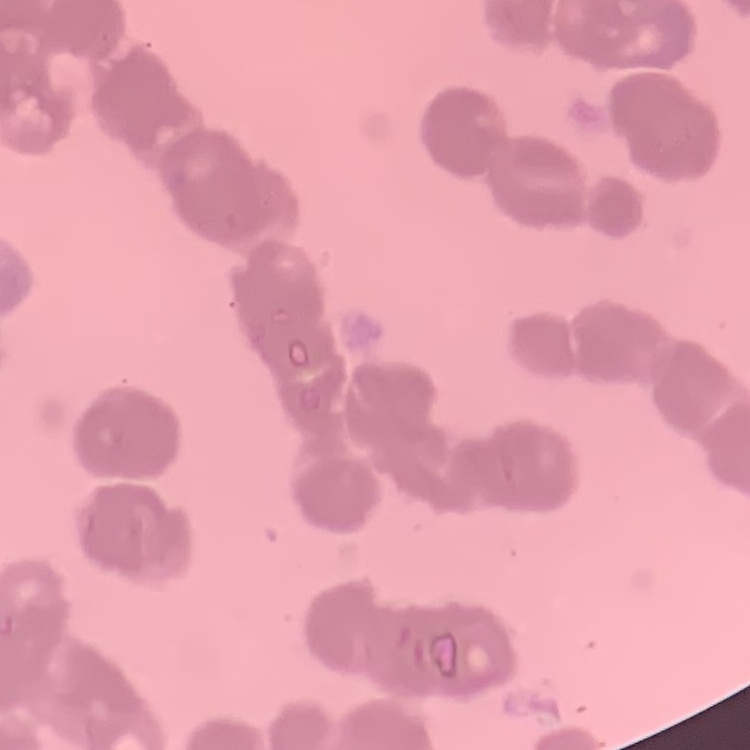
The erythrocytes exhibit rouleaux formation. Square crop of a larger photomicrograph. Stained with either Field's or Giemsa. Thin blood smear.